Outline each Plasmodium malariae-infected red blood cell.
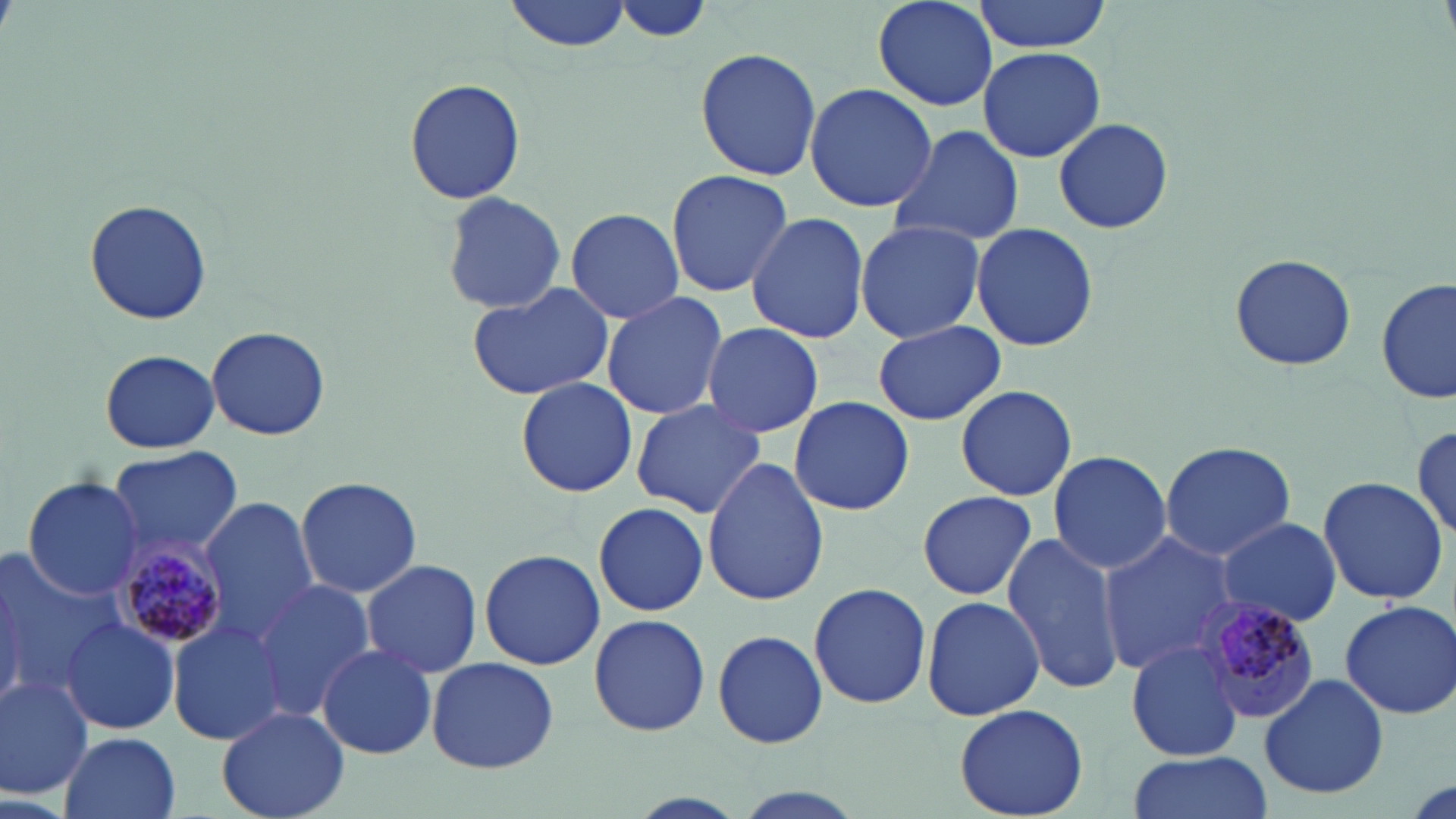
Approximate bounding boxes as named x1/y1/x2/y2 corners in pixels.
Plasmodium malariae-infected red blood cells: (x1=115, y1=541, x2=230, y2=650), (x1=1198, y1=595, x2=1321, y2=724).

Uninfected red blood cell locations: (x1=504, y1=0, x2=630, y2=53), (x1=614, y1=0, x2=714, y2=47), (x1=872, y1=0, x2=1003, y2=111), (x1=973, y1=0, x2=1110, y2=53), (x1=977, y1=46, x2=1105, y2=164), (x1=695, y1=48, x2=822, y2=180), (x1=404, y1=76, x2=526, y2=207), (x1=803, y1=82, x2=936, y2=213), (x1=1053, y1=117, x2=1173, y2=235), (x1=887, y1=125, x2=1026, y2=249), (x1=665, y1=170, x2=793, y2=296), (x1=439, y1=192, x2=568, y2=316), (x1=83, y1=201, x2=213, y2=325), (x1=565, y1=206, x2=686, y2=323), (x1=745, y1=211, x2=871, y2=344), (x1=854, y1=219, x2=987, y2=344), (x1=971, y1=222, x2=1100, y2=352), (x1=1229, y1=253, x2=1357, y2=372), (x1=1377, y1=279, x2=1453, y2=405), (x1=466, y1=280, x2=616, y2=402), (x1=601, y1=290, x2=730, y2=421), (x1=870, y1=322, x2=1008, y2=425), (x1=701, y1=323, x2=825, y2=439), (x1=205, y1=325, x2=332, y2=441), (x1=99, y1=349, x2=220, y2=453), (x1=515, y1=378, x2=637, y2=497), (x1=953, y1=385, x2=1079, y2=501), (x1=787, y1=396, x2=914, y2=515), (x1=628, y1=399, x2=768, y2=520), (x1=1412, y1=422, x2=1454, y2=540), (x1=1160, y1=441, x2=1294, y2=561), (x1=108, y1=445, x2=243, y2=560), (x1=1047, y1=449, x2=1173, y2=574), (x1=702, y1=456, x2=830, y2=605), (x1=256, y1=472, x2=412, y2=677), (x1=294, y1=475, x2=422, y2=599), (x1=22, y1=476, x2=148, y2=600), (x1=1318, y1=477, x2=1449, y2=606), (x1=918, y1=490, x2=1036, y2=601), (x1=202, y1=498, x2=322, y2=637), (x1=593, y1=500, x2=708, y2=617), (x1=1216, y1=517, x2=1342, y2=626), (x1=1099, y1=531, x2=1243, y2=675), (x1=1000, y1=535, x2=1125, y2=696), (x1=480, y1=548, x2=605, y2=671), (x1=1, y1=550, x2=127, y2=694), (x1=362, y1=561, x2=483, y2=677), (x1=248, y1=579, x2=375, y2=720), (x1=809, y1=580, x2=932, y2=710), (x1=921, y1=595, x2=1045, y2=721), (x1=1339, y1=599, x2=1456, y2=718), (x1=589, y1=612, x2=710, y2=737), (x1=168, y1=616, x2=292, y2=746), (x1=61, y1=618, x2=180, y2=735), (x1=712, y1=629, x2=828, y2=750), (x1=1126, y1=641, x2=1246, y2=760), (x1=316, y1=645, x2=439, y2=759), (x1=427, y1=655, x2=558, y2=774), (x1=0, y1=674, x2=95, y2=798), (x1=1258, y1=674, x2=1391, y2=799), (x1=954, y1=704, x2=1089, y2=818), (x1=219, y1=706, x2=349, y2=818), (x1=58, y1=731, x2=181, y2=819), (x1=1124, y1=752, x2=1275, y2=819). Slide-level diagnosis: Plasmodium malariae. 1000x magnification. Light microscopy. One field of a larger specimen. May-Grünwald-Giemsa-stained preparation. Image is 1456×819 pixels. Thin blood smear.